Classify this cell by malaria status.
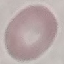

It is uninfected.

Summary:
  - Image type: automatically extracted cell patch, resized to 64 × 64 pixels
  - Capture: smartphone through the microscope eyepiece
  - Stain: Giemsa
  - Preparation: thin smear